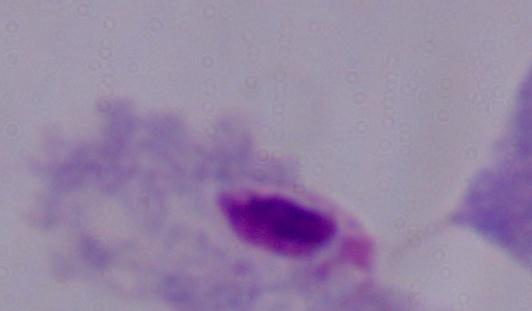

modality = photomicrograph
magnification = 1000x
identification = trichomonad